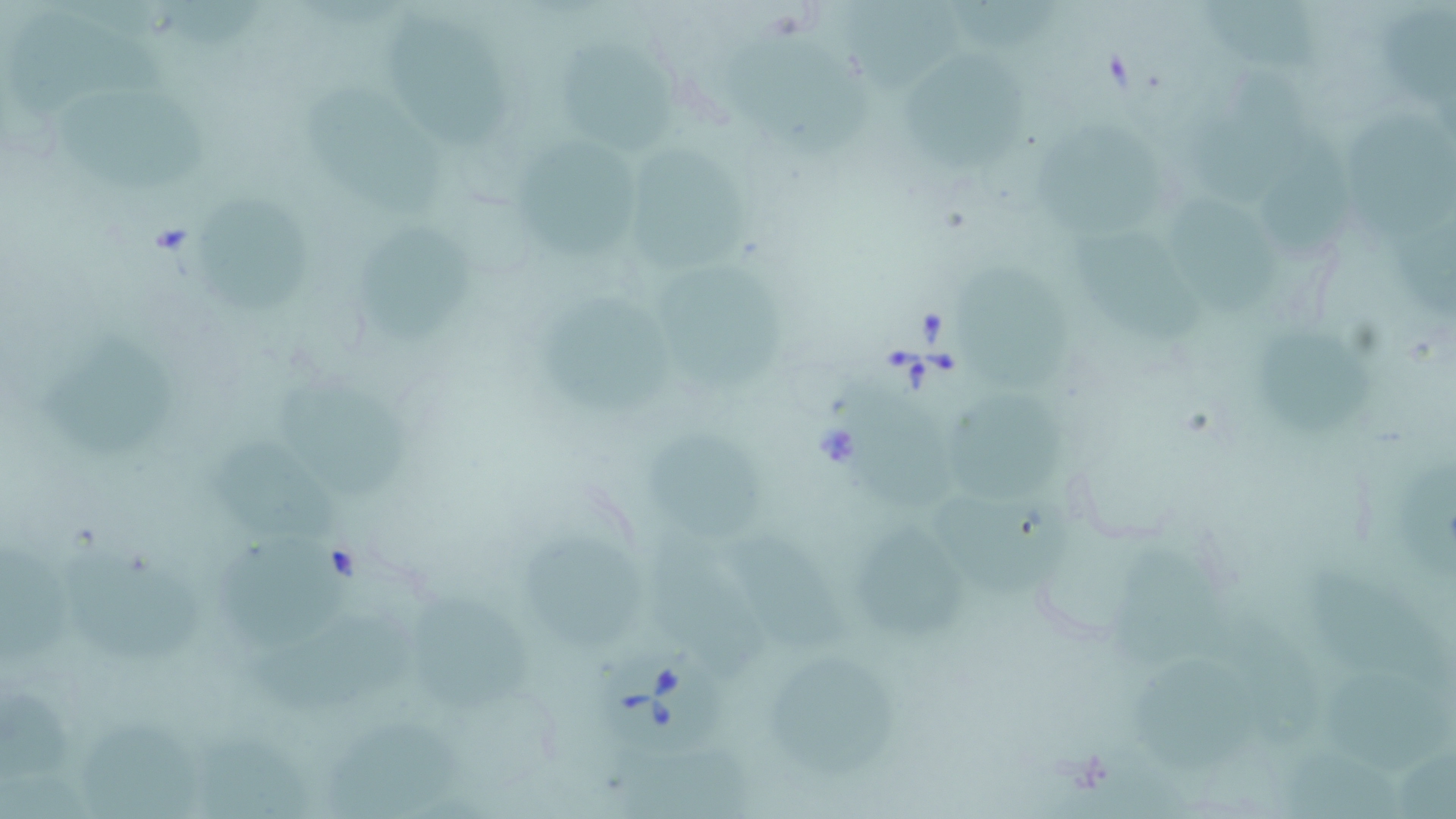

slide-level diagnosis = Babesia divergens
stain = May-Grünwald-Giemsa
magnification = 1000x
image size = 1456×819 pixels
preparation = thin blood film
uninfected red blood cell locations = approximate bounding boxes as named x1/y1/x2/y2 corners in pixels: (x1=1385, y1=0, x2=1456, y2=116), (x1=155, y1=2, x2=280, y2=57), (x1=847, y1=2, x2=968, y2=96), (x1=1185, y1=5, x2=1334, y2=85), (x1=385, y1=14, x2=508, y2=148), (x1=11, y1=18, x2=176, y2=123), (x1=735, y1=35, x2=867, y2=151), (x1=562, y1=45, x2=685, y2=151), (x1=901, y1=45, x2=1026, y2=168), (x1=1188, y1=78, x2=1311, y2=202), (x1=304, y1=88, x2=440, y2=223), (x1=60, y1=90, x2=218, y2=190), (x1=1031, y1=104, x2=1165, y2=238), (x1=1345, y1=114, x2=1456, y2=245), (x1=1267, y1=121, x2=1354, y2=254), (x1=527, y1=139, x2=653, y2=258), (x1=631, y1=149, x2=764, y2=279), (x1=1166, y1=191, x2=1280, y2=317), (x1=194, y1=195, x2=324, y2=317), (x1=1389, y1=210, x2=1456, y2=324), (x1=1071, y1=226, x2=1205, y2=344), (x1=358, y1=227, x2=485, y2=351), (x1=961, y1=269, x2=1081, y2=393), (x1=657, y1=274, x2=786, y2=395), (x1=542, y1=287, x2=684, y2=419), (x1=1264, y1=328, x2=1374, y2=439), (x1=43, y1=333, x2=174, y2=458), (x1=267, y1=377, x2=413, y2=505), (x1=839, y1=377, x2=965, y2=513), (x1=952, y1=393, x2=1077, y2=499), (x1=637, y1=431, x2=772, y2=537), (x1=227, y1=440, x2=342, y2=549), (x1=1394, y1=454, x2=1456, y2=570), (x1=940, y1=483, x2=1071, y2=600), (x1=859, y1=525, x2=969, y2=633), (x1=217, y1=529, x2=359, y2=650), (x1=525, y1=533, x2=657, y2=652), (x1=646, y1=534, x2=778, y2=680), (x1=721, y1=537, x2=859, y2=652), (x1=0, y1=538, x2=70, y2=672), (x1=1117, y1=546, x2=1232, y2=674), (x1=60, y1=547, x2=206, y2=668), (x1=1298, y1=562, x2=1453, y2=688), (x1=413, y1=598, x2=536, y2=714), (x1=252, y1=612, x2=421, y2=719), (x1=1224, y1=624, x2=1326, y2=746), (x1=1130, y1=657, x2=1256, y2=786), (x1=774, y1=659, x2=906, y2=780), (x1=1323, y1=675, x2=1453, y2=774), (x1=0, y1=687, x2=75, y2=789), (x1=84, y1=715, x2=214, y2=819), (x1=323, y1=722, x2=472, y2=819), (x1=1278, y1=729, x2=1408, y2=819), (x1=202, y1=731, x2=308, y2=819), (x1=606, y1=739, x2=753, y2=819), (x1=1397, y1=754, x2=1456, y2=819)
Babesia divergens-infected red blood cell locations = approximate bounding boxes as named x1/y1/x2/y2 corners in pixels: (x1=598, y1=648, x2=737, y2=758)
field of view = single
modality = light microscopy